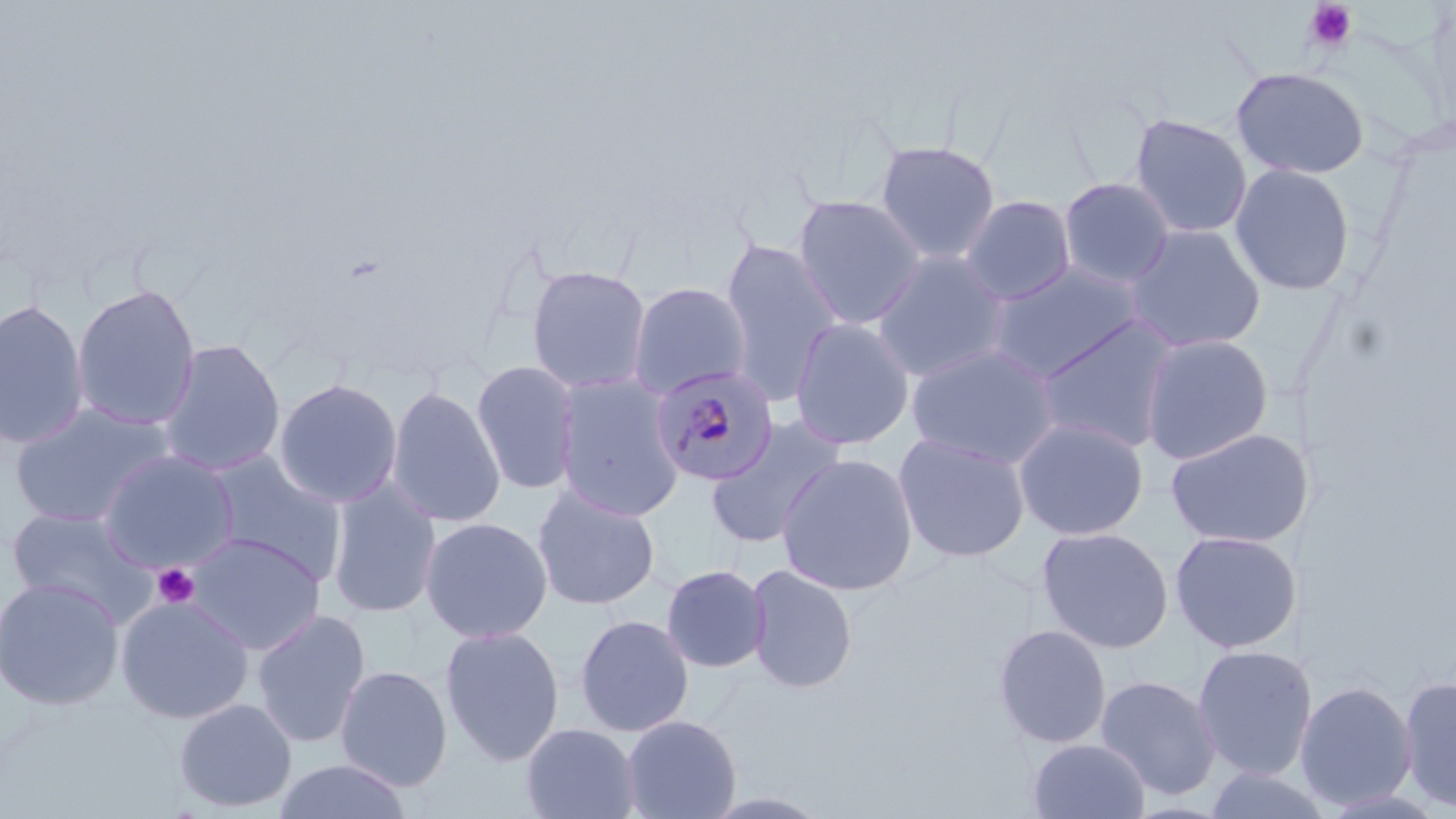

Summary:
  - Coordinate format: approximate bounding boxes as (x1, y1, x2, y2) in pixels
  - Platelet locations: (1303, 1, 1359, 53), (152, 563, 199, 608)
  - Plasmodium malariae-infected red blood cell locations: (651, 364, 779, 486)
  - Uninfected red blood cell locations: (1230, 66, 1370, 180), (1129, 113, 1253, 240), (874, 140, 1002, 265), (1229, 163, 1357, 297), (1058, 176, 1175, 288), (792, 194, 927, 329), (959, 195, 1077, 305), (1122, 223, 1267, 353), (719, 238, 844, 405), (871, 249, 1011, 383), (987, 262, 1144, 381), (525, 266, 652, 395), (627, 281, 753, 399), (71, 282, 201, 432), (0, 298, 90, 450), (1034, 315, 1182, 454), (789, 317, 915, 451), (1138, 332, 1275, 464), (157, 338, 286, 476), (906, 344, 1060, 469), (471, 359, 582, 495), (552, 374, 686, 521), (273, 378, 403, 508), (386, 385, 506, 528), (8, 402, 174, 528), (704, 415, 849, 551), (1013, 417, 1149, 541), (1165, 427, 1304, 548), (893, 433, 1031, 563), (98, 449, 239, 573), (203, 452, 345, 583), (775, 452, 919, 596), (326, 480, 442, 620), (531, 484, 660, 611), (5, 507, 157, 624), (419, 516, 553, 643), (1036, 526, 1175, 654), (1169, 530, 1301, 653), (185, 532, 325, 655), (660, 563, 771, 673), (744, 564, 859, 693), (0, 575, 125, 711), (115, 594, 254, 724), (251, 608, 372, 748), (574, 614, 695, 737), (992, 623, 1113, 749), (439, 625, 565, 766), (1191, 644, 1306, 780), (335, 665, 453, 792), (1095, 674, 1221, 799), (1398, 675, 1456, 812), (1301, 679, 1417, 810), (172, 698, 298, 814), (620, 714, 742, 819), (519, 723, 641, 819), (1027, 737, 1151, 819), (271, 758, 415, 819), (1203, 764, 1327, 819)
  - Slide-level diagnosis: Plasmodium malariae
  - Magnification: 1000x
  - Stain: May-Grünwald-Giemsa
  - Preparation: thin blood smear
  - Field of view: one of a larger specimen
  - Modality: light microscopy
  - Image size: 1456×819 pixels